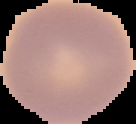 Segmented cell region on a black background. Malaria status: uninfected. From a thin blood smear. Image is 136×124 pixels.